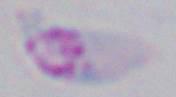

magnification: 1000x
modality: micrograph
identification: Toxoplasma gondii